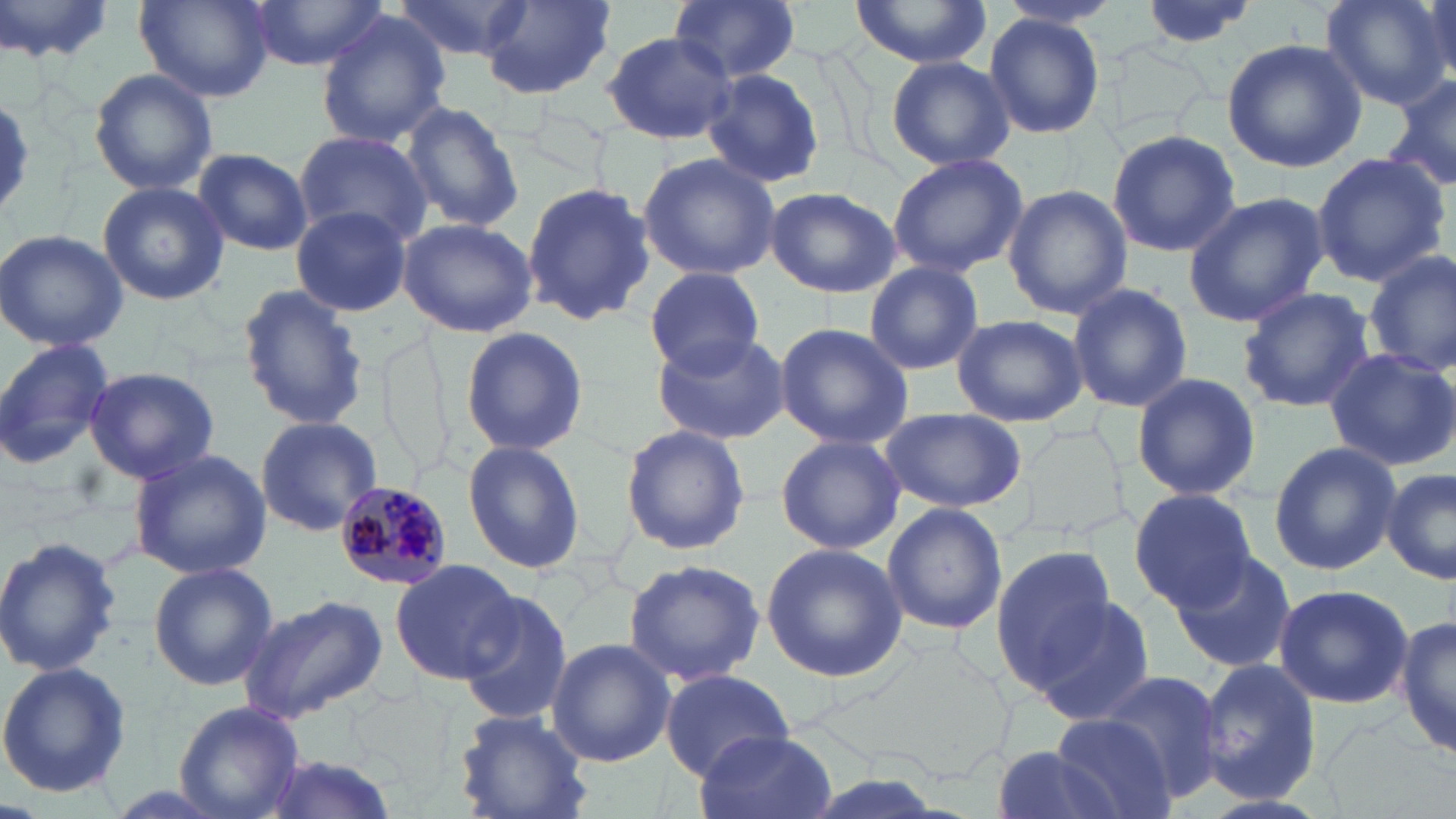
slide_level_diagnosis: Plasmodium malariae
stain: May-Grünwald-Giemsa
magnification: 1000x
modality: light microscopy
uninfected_red_blood_cell_locations: 'approximate bounding boxes as (x1, y1, x2, y2) in pixels: (137, 0, 274, 101), (244, 0, 384, 69), (389, 0, 533, 63), (476, 0, 617, 101), (668, 0, 801, 81), (849, 0, 993, 71), (1132, 0, 1260, 49), (1319, 0, 1450, 109), (1421, 0, 1456, 92), (0, 1, 119, 65), (984, 13, 1106, 140), (317, 14, 451, 150), (599, 30, 737, 145), (1222, 39, 1368, 173), (885, 55, 1014, 171), (699, 65, 826, 189), (88, 67, 219, 196), (1383, 72, 1456, 198), (400, 101, 525, 235), (1107, 128, 1240, 256), (291, 129, 431, 247), (193, 148, 313, 256), (637, 152, 781, 282), (1308, 152, 1450, 286), (884, 153, 1028, 279), (98, 181, 229, 306), (521, 182, 657, 327), (1002, 185, 1131, 320), (766, 186, 899, 297), (1181, 192, 1328, 326), (292, 207, 412, 316), (397, 217, 537, 338), (0, 228, 129, 352), (1362, 251, 1456, 378), (860, 262, 985, 375), (642, 268, 771, 377), (1065, 283, 1194, 413), (237, 284, 369, 432), (1235, 285, 1375, 414), (949, 314, 1088, 426), (774, 322, 915, 448), (460, 325, 590, 457), (652, 328, 791, 444), (0, 338, 116, 469), (1323, 348, 1456, 469), (81, 366, 220, 484), (1130, 373, 1261, 502), (879, 408, 1027, 513), (255, 415, 381, 537), (621, 424, 750, 556), (776, 433, 905, 555), (462, 441, 586, 575), (1268, 442, 1401, 576), (129, 449, 271, 579), (1382, 469, 1455, 583), (1129, 488, 1254, 611), (881, 500, 1008, 636), (0, 535, 124, 679), (760, 541, 908, 682), (1170, 546, 1301, 674), (989, 547, 1118, 687), (390, 559, 520, 684), (623, 560, 766, 684), (148, 562, 278, 690), (1273, 583, 1413, 709), (457, 590, 574, 724), (239, 593, 388, 723), (1028, 595, 1160, 726), (1395, 616, 1454, 762), (546, 637, 674, 766), (1197, 659, 1322, 804), (0, 661, 131, 798), (661, 668, 793, 776), (1097, 670, 1221, 796), (174, 701, 305, 818), (453, 709, 593, 819), (1052, 713, 1177, 819), (691, 732, 836, 819), (990, 745, 1126, 819), (254, 753, 405, 819)'
plasmodium_malariae_infected_red_blood_cell_locations: 'approximate bounding boxes as (x1, y1, x2, y2) in pixels: (339, 482, 449, 591)'
image_size: 1456×819 pixels
preparation: thin blood film
field_of_view: one of a larger specimen